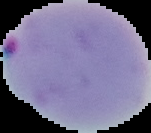

Cell region segmented out of the field of view; the surrounding area is masked to black. Result: Plasmodium parasites detected. From a thin blood film. Image is 151×133 pixels.